Report the malaria status of this cell.
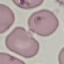

Uninfected.

Giemsa stain. Thin blood film. Cell patch, automatically extracted from a larger field of view and resized to 64 × 64 pixels. Acquired by smartphone through the microscope eyepiece.